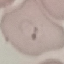
malaria_status: parasitized
stain: Giemsa
preparation: thin smear
capture: smartphone through the microscope eyepiece
image_type: cell patch, automatically extracted from a larger field of view and resized to 64 × 64 pixels